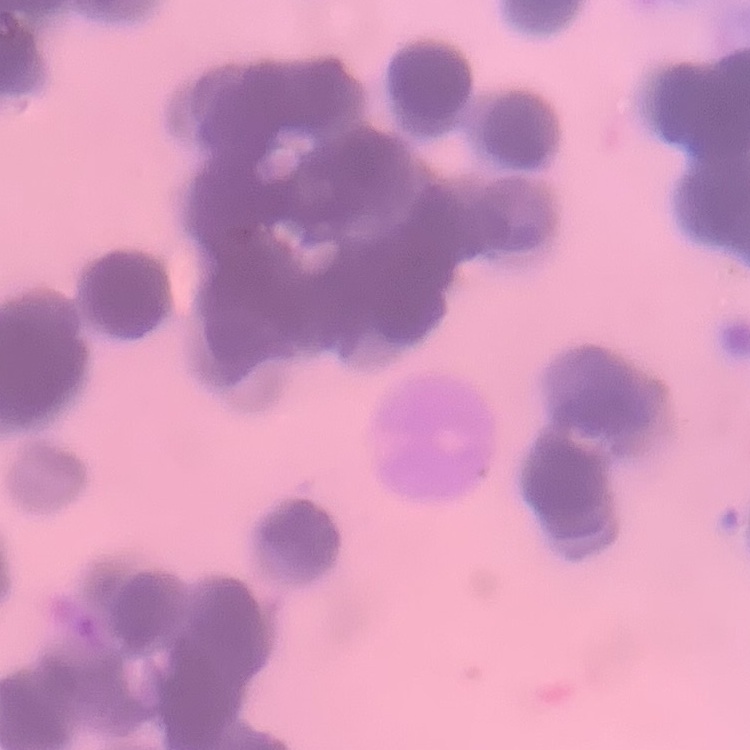

{
  "red_blood_cell_morphology": "rouleaux formation",
  "preparation": "thin blood smear",
  "stain": "Field's or Giemsa",
  "image_type": "square crop of a larger photomicrograph"
}